Classify this cell by malaria status.
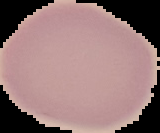

It is uninfected.

The area outside the segmented cell region is set to black. Image is 160×133 pixels. From a thin blood smear.